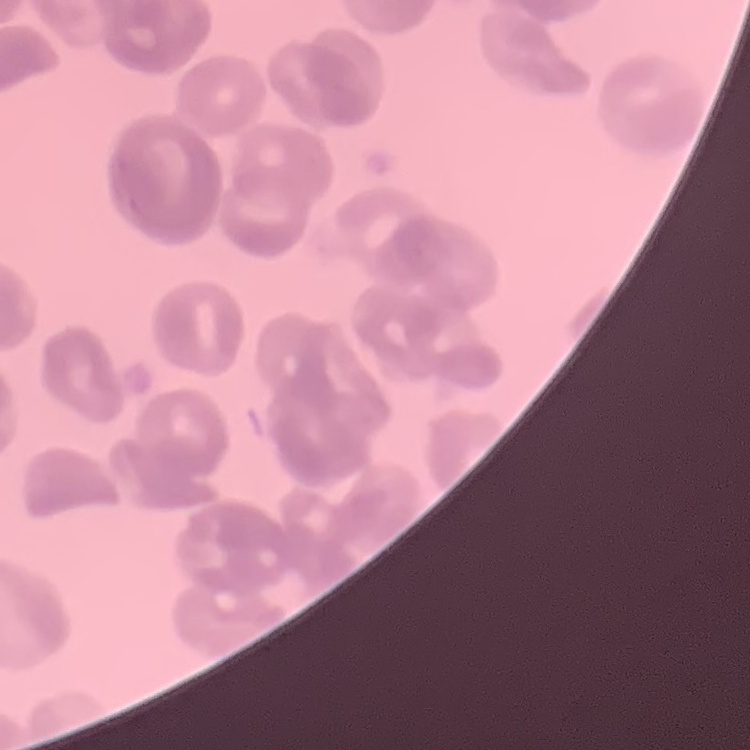

Summary:
  - Erythrocyte morphology: rouleaux formation
  - Stain: Field's or Giemsa
  - Preparation: thin blood film
  - Image type: one tile cut from a larger photomicrograph